Locate every leukocyte (white blood cell).
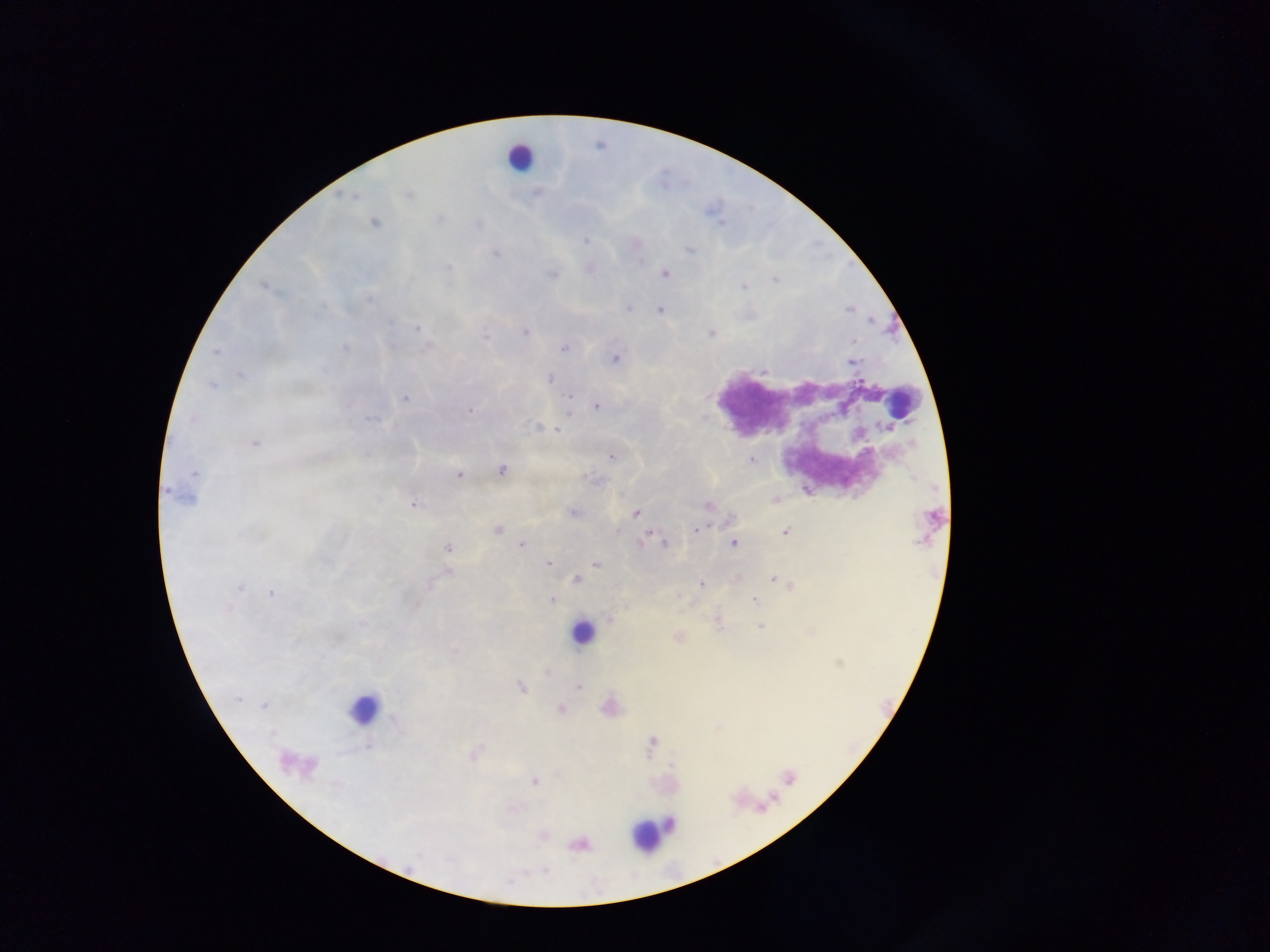
Approximate centers as (x, y) in pixels.
Leukocytes: (520, 156), (902, 402), (583, 631), (363, 708), (650, 832).

Summary:
  - Plasmodium parasite locations: (538, 194), (407, 195), (438, 218), (374, 223), (584, 240), (688, 248), (495, 253), (591, 269), (664, 273), (552, 274), (627, 307), (661, 310), (416, 328), (525, 331), (710, 333), (486, 337), (344, 348), (565, 348), (614, 358), (852, 361), (239, 375), (551, 378), (211, 385), (406, 399), (596, 406), (471, 409), (536, 427), (558, 429), (253, 441), (367, 455), (611, 456), (750, 459), (501, 469), (194, 473), (458, 474), (181, 494), (775, 499), (414, 503), (708, 506), (572, 512), (635, 513), (497, 529), (695, 530), (785, 531), (641, 541), (733, 542), (664, 544), (521, 545), (448, 548), (548, 564), (596, 564), (448, 572), (576, 579), (773, 579), (700, 584), (789, 585), (239, 588), (271, 592), (551, 599), (754, 599), (717, 618), (608, 619), (362, 624), (760, 625), (678, 637), (454, 650), (547, 671), (577, 686), (520, 688), (609, 707), (559, 708), (651, 741), (474, 753), (535, 781), (542, 834), (579, 844)
  - Image size: 1270×952 pixels
  - Preparation: thick blood film
  - Capture: mobile-phone photograph through a microscope
  - Field of view: single
  - Country: Ghana